Assess this cell for malaria.
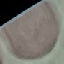

Uninfected.

Acquired by smartphone through the microscope eyepiece. Automatically extracted cell patch, resized to 64 × 64 pixels. Giemsa stain. Thin blood film.